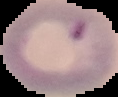
Result: Plasmodium parasites identified. Image is 118×97 pixels. From a thin blood film. The area outside the segmented cell region is set to black.